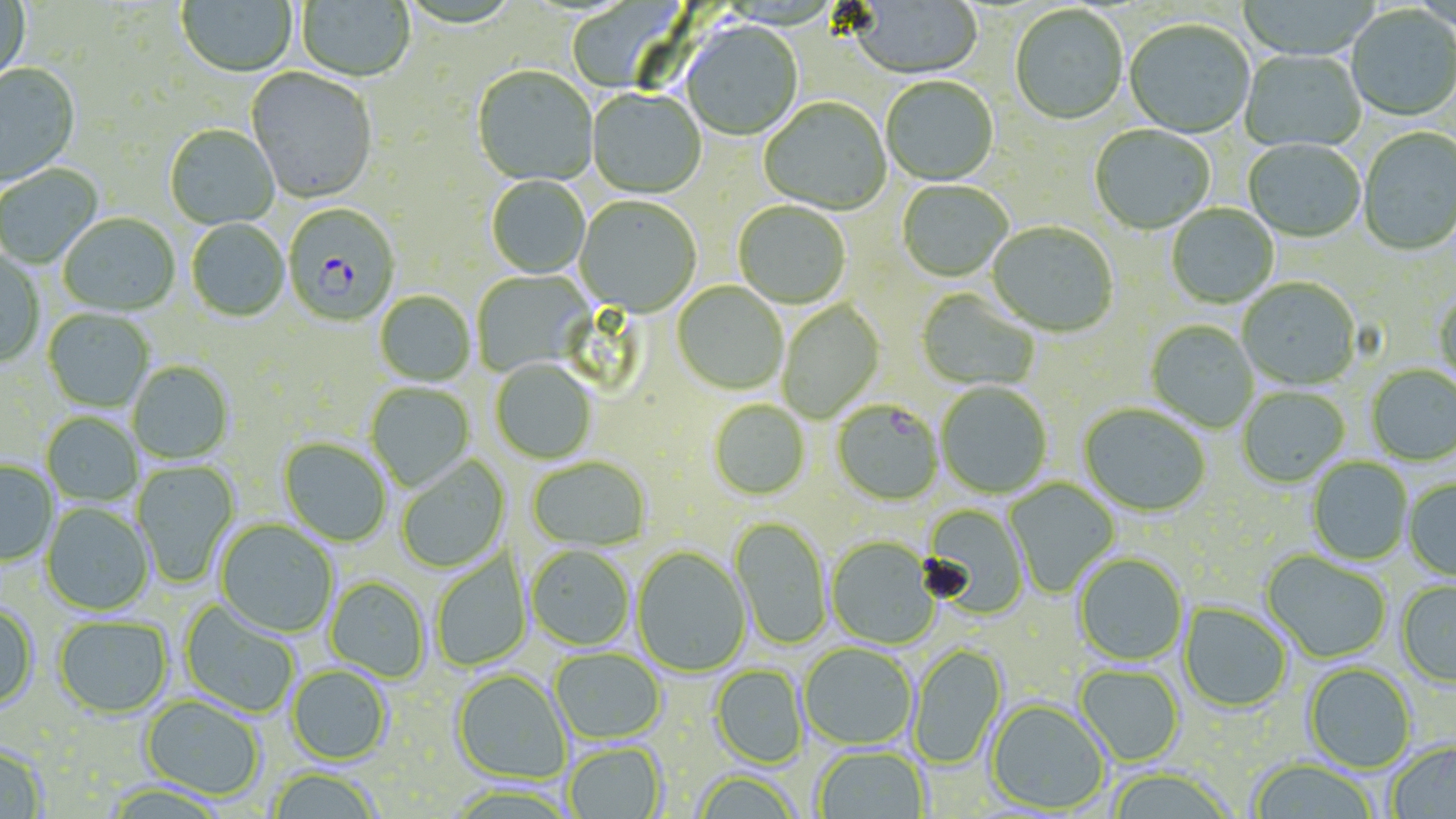
slide_level_diagnosis: Plasmodium falciparum
uninfected_red_blood_cell_locations: 'approximate bounding boxes as named x1/y1/x2/y2 corners in pixels: (x1=0, y1=0, x2=31, y2=90), (x1=176, y1=0, x2=297, y2=79), (x1=296, y1=1, x2=414, y2=84), (x1=847, y1=1, x2=983, y2=81), (x1=566, y1=2, x2=692, y2=94), (x1=1010, y1=6, x2=1128, y2=127), (x1=1346, y1=6, x2=1456, y2=123), (x1=1124, y1=21, x2=1255, y2=139), (x1=680, y1=23, x2=803, y2=142), (x1=1240, y1=50, x2=1366, y2=153), (x1=0, y1=64, x2=82, y2=190), (x1=471, y1=67, x2=598, y2=187), (x1=245, y1=68, x2=378, y2=206), (x1=882, y1=78, x2=999, y2=187), (x1=586, y1=90, x2=706, y2=200), (x1=759, y1=98, x2=892, y2=217), (x1=165, y1=126, x2=280, y2=230), (x1=1090, y1=126, x2=1215, y2=236), (x1=1359, y1=129, x2=1456, y2=257), (x1=1243, y1=140, x2=1365, y2=244), (x1=0, y1=164, x2=103, y2=270), (x1=486, y1=176, x2=590, y2=280), (x1=897, y1=181, x2=1013, y2=284), (x1=574, y1=197, x2=701, y2=318), (x1=733, y1=203, x2=851, y2=310), (x1=1166, y1=205, x2=1279, y2=309), (x1=58, y1=214, x2=180, y2=318), (x1=186, y1=220, x2=290, y2=323), (x1=986, y1=223, x2=1118, y2=338), (x1=0, y1=251, x2=45, y2=368), (x1=471, y1=270, x2=594, y2=377), (x1=1238, y1=279, x2=1361, y2=391), (x1=672, y1=282, x2=788, y2=396), (x1=1434, y1=288, x2=1456, y2=392), (x1=916, y1=289, x2=1040, y2=392), (x1=374, y1=292, x2=475, y2=388), (x1=778, y1=299, x2=885, y2=423), (x1=43, y1=310, x2=154, y2=413), (x1=1145, y1=321, x2=1258, y2=433), (x1=490, y1=360, x2=597, y2=465), (x1=128, y1=362, x2=233, y2=465), (x1=1367, y1=366, x2=1456, y2=466), (x1=365, y1=383, x2=475, y2=492), (x1=936, y1=383, x2=1052, y2=499), (x1=1237, y1=387, x2=1349, y2=488), (x1=709, y1=401, x2=810, y2=501), (x1=1078, y1=405, x2=1210, y2=518), (x1=42, y1=414, x2=143, y2=507), (x1=277, y1=437, x2=392, y2=548), (x1=396, y1=455, x2=510, y2=573), (x1=527, y1=457, x2=651, y2=554), (x1=1307, y1=458, x2=1413, y2=566), (x1=132, y1=459, x2=240, y2=587), (x1=0, y1=461, x2=58, y2=567), (x1=1005, y1=478, x2=1120, y2=597), (x1=1404, y1=478, x2=1456, y2=582), (x1=41, y1=503, x2=155, y2=617), (x1=921, y1=504, x2=1030, y2=619), (x1=728, y1=517, x2=832, y2=652), (x1=214, y1=519, x2=338, y2=639), (x1=825, y1=537, x2=940, y2=650), (x1=526, y1=547, x2=634, y2=652), (x1=631, y1=547, x2=752, y2=678), (x1=1261, y1=551, x2=1391, y2=663), (x1=431, y1=553, x2=533, y2=670), (x1=1074, y1=554, x2=1188, y2=667), (x1=324, y1=576, x2=429, y2=683), (x1=1396, y1=581, x2=1456, y2=688), (x1=180, y1=600, x2=300, y2=718), (x1=0, y1=603, x2=39, y2=712), (x1=1178, y1=603, x2=1292, y2=713), (x1=53, y1=616, x2=173, y2=719), (x1=908, y1=644, x2=1008, y2=770), (x1=799, y1=645, x2=917, y2=751), (x1=551, y1=649, x2=665, y2=745), (x1=1303, y1=663, x2=1416, y2=773), (x1=709, y1=664, x2=808, y2=770), (x1=1074, y1=665, x2=1184, y2=767), (x1=286, y1=666, x2=392, y2=766), (x1=451, y1=670, x2=571, y2=786), (x1=140, y1=696, x2=265, y2=802), (x1=985, y1=700, x2=1110, y2=815), (x1=1385, y1=741, x2=1456, y2=819), (x1=0, y1=743, x2=48, y2=818), (x1=564, y1=743, x2=667, y2=819), (x1=814, y1=747, x2=930, y2=819), (x1=1248, y1=758, x2=1379, y2=819), (x1=1105, y1=768, x2=1235, y2=819), (x1=267, y1=770, x2=381, y2=818), (x1=692, y1=773, x2=802, y2=818)'
field_of_view: one of a larger specimen
magnification: 1000x
modality: light microscopy
image_size: 1456×819 pixels
stain: May-Grünwald-Giemsa
plasmodium_falciparum_infected_red_blood_cell_locations: 'approximate bounding boxes as named x1/y1/x2/y2 corners in pixels: (x1=282, y1=205, x2=400, y2=328), (x1=832, y1=401, x2=944, y2=507)'
preparation: thin blood film